Classify this cell by malaria status.
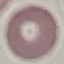
Uninfected.

{
  "image_type": "cell patch, automatically extracted from a larger field of view and resized to 64 × 64 pixels",
  "preparation": "thin blood smear",
  "stain": "Giemsa",
  "capture": "smartphone through the microscope eyepiece"
}